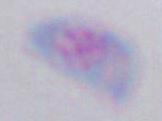
Micrograph. Captured at 1000x magnification. Toxoplasma gondii is shown.